Give the extent of all uninfected red blood cells.
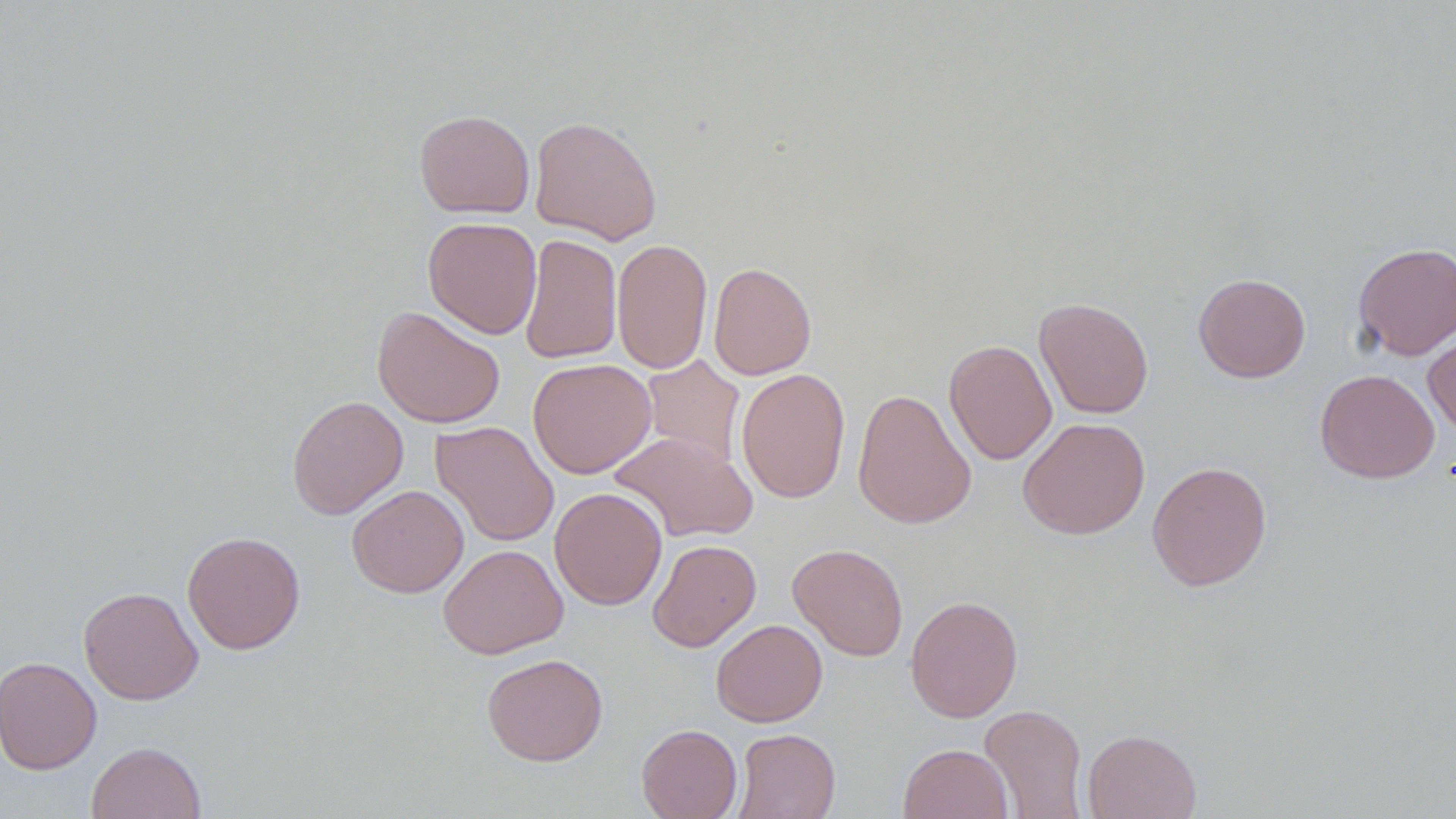
Approximate bounding boxes as [x1, y1, x2, y2] in pixels.
Uninfected red blood cells: [414, 109, 535, 219], [529, 115, 663, 245], [423, 216, 542, 339], [518, 233, 622, 365], [612, 237, 713, 375], [1352, 242, 1456, 359], [708, 262, 816, 380], [1193, 273, 1311, 383], [1034, 297, 1154, 419], [372, 306, 505, 428], [1423, 324, 1456, 438], [944, 339, 1057, 464], [640, 355, 745, 470], [527, 358, 656, 479], [736, 367, 851, 503], [1315, 369, 1439, 483], [852, 387, 977, 530], [286, 395, 408, 519], [1017, 416, 1150, 539], [431, 421, 559, 547], [610, 432, 758, 543], [1147, 461, 1272, 591], [347, 484, 469, 598], [550, 487, 667, 610], [182, 531, 306, 654], [647, 539, 761, 652], [788, 542, 909, 660], [438, 543, 568, 659], [78, 586, 203, 705], [905, 594, 1023, 722], [711, 618, 827, 727], [482, 652, 608, 767], [1, 655, 102, 775], [979, 703, 1089, 818], [637, 723, 742, 819], [732, 728, 841, 819], [1082, 729, 1202, 819], [86, 741, 207, 819], [898, 743, 1012, 819].

Slide-level diagnosis: negative for blood parasites. Single field of view. Image is 1456×819 pixels. Captured at 1000x magnification. May-Grünwald-Giemsa stain. Optical microscopy. Thin blood smear.